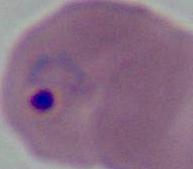

Summary:
  - Modality: micrograph
  - Identification: Plasmodium
  - Magnification: 400x or 1000x